Describe the morphology of the erythrocytes.
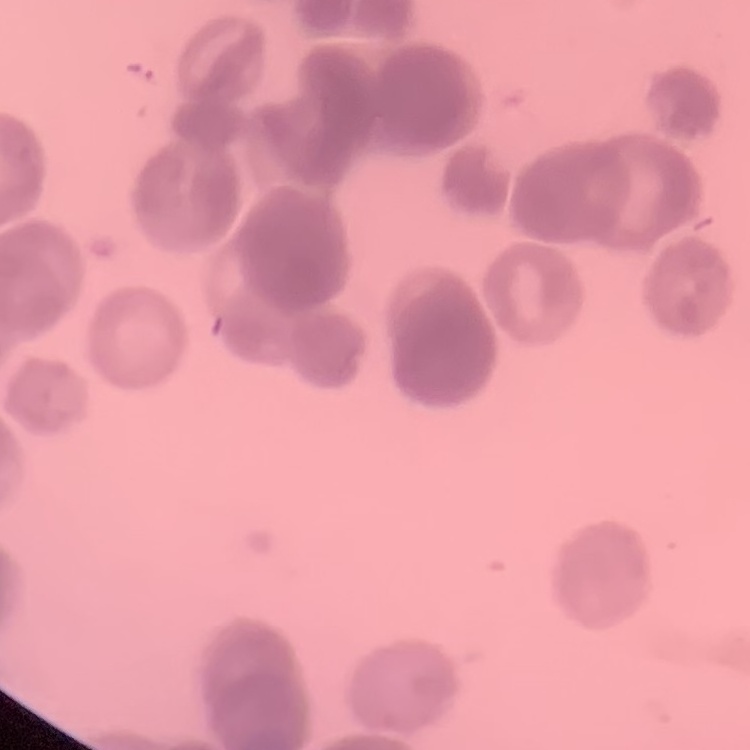
They show rouleaux formation.

One tile cut from a larger photomicrograph. Thin peripheral smear. Field's or Giemsa stain.